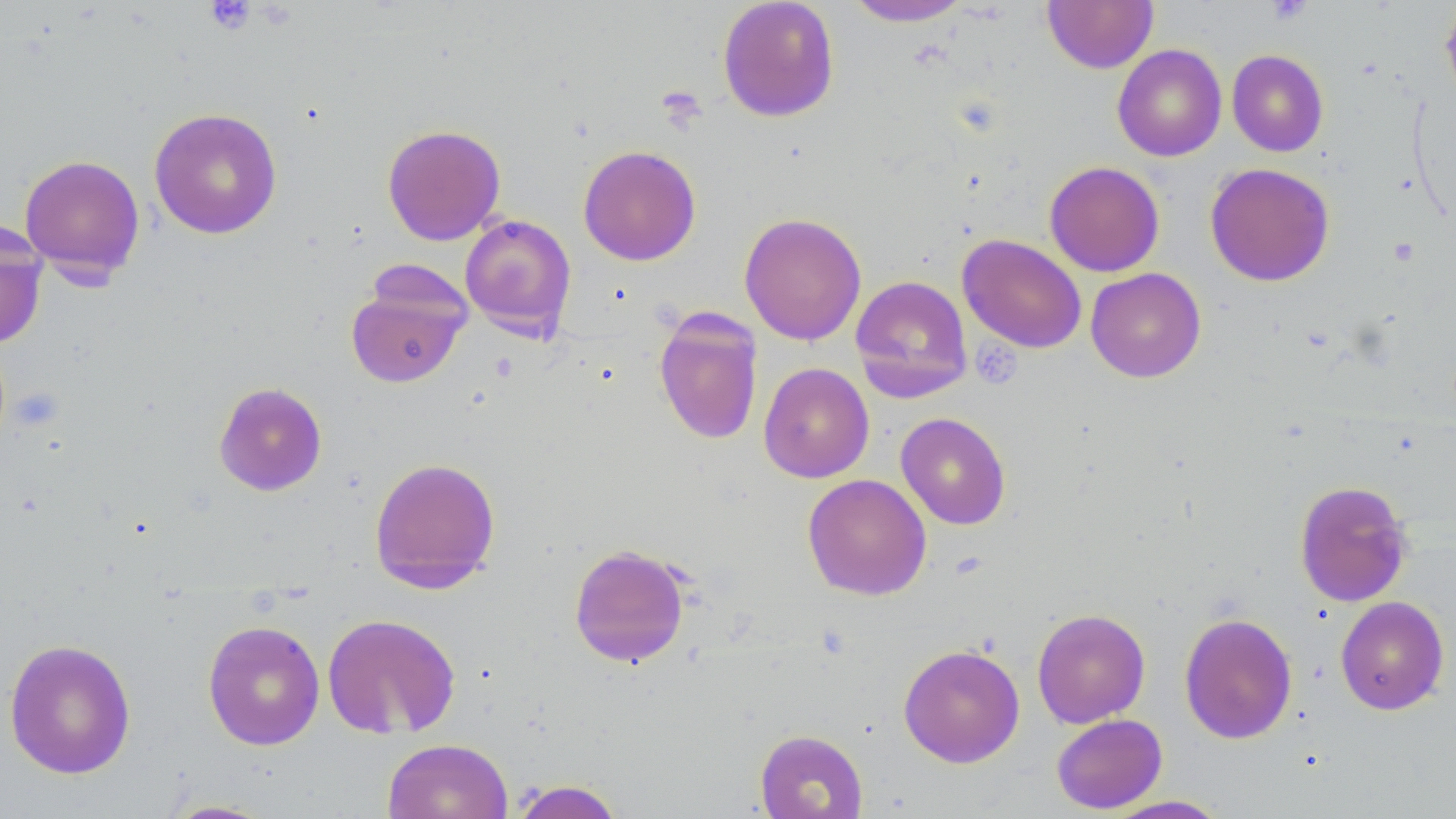

Summary:
  - Coordinate format: approximate bounding boxes as (x1,y1)-(x2,y2) corner pairs in pixels
  - Platelet locations: (1266,0)-(1313,25), (206,1)-(257,35), (657,86)-(707,130), (976,341)-(1024,388)
  - Uninfected red blood cell locations: (843,0)-(975,27), (1043,0)-(1159,74), (717,1)-(840,122), (1440,2)-(1456,107), (1112,44)-(1227,162), (1227,50)-(1329,157), (148,107)-(283,239), (382,123)-(506,246), (577,145)-(702,266), (19,153)-(146,282), (1044,161)-(1164,277), (1205,163)-(1335,286), (739,212)-(867,346), (459,213)-(576,340), (0,221)-(48,350), (957,234)-(1087,354), (1085,267)-(1206,383), (345,274)-(470,389), (850,275)-(973,403), (653,308)-(764,446), (758,362)-(874,483), (214,382)-(327,496), (895,412)-(1011,530), (369,456)-(501,593), (802,473)-(932,600), (1294,480)-(1414,607), (568,543)-(692,668), (1335,596)-(1450,715), (1032,608)-(1150,728), (1179,612)-(1298,744), (322,613)-(461,739), (202,619)-(325,750), (3,638)-(137,779), (898,643)-(1025,768), (1051,713)-(1168,814), (754,729)-(868,819), (382,738)-(513,819), (508,779)-(626,819), (1101,795)-(1231,818), (159,799)-(278,818)
  - Slide-level diagnosis: no evidence of blood parasites
  - Image size: 1456×819 pixels
  - Stain: May-Grünwald-Giemsa
  - Preparation: thin blood smear
  - Field of view: one of a larger specimen
  - Magnification: 1000x
  - Modality: light microscopy